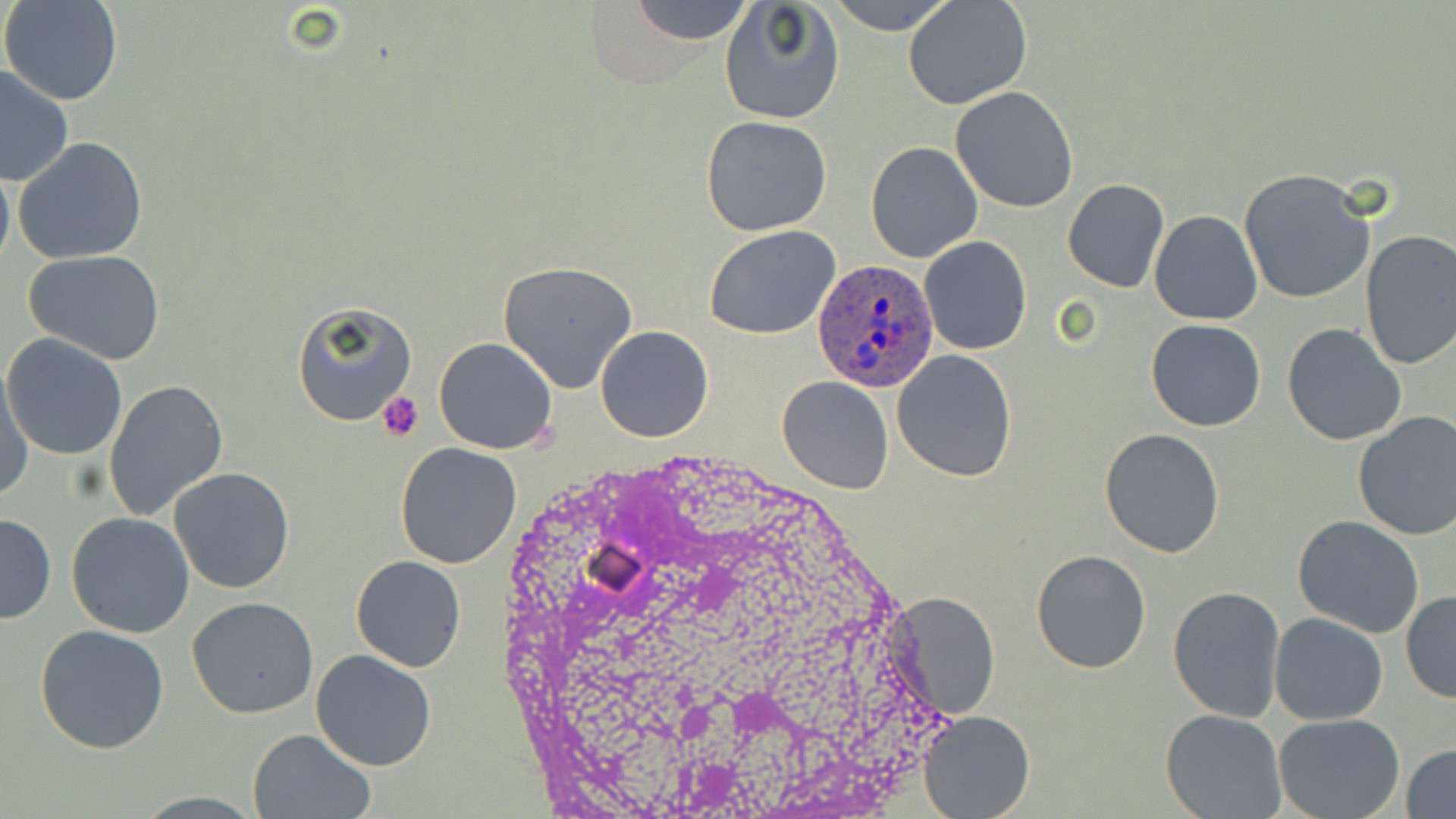
slide-level diagnosis = Plasmodium ovale
uninfected red blood cell locations = approximate bounding boxes as (x1, y1, x2, y2) in pixels: (2, 0, 124, 107), (628, 0, 755, 44), (826, 0, 958, 36), (904, 0, 1033, 109), (718, 2, 845, 125), (0, 65, 76, 188), (949, 86, 1079, 213), (700, 115, 833, 237), (14, 137, 148, 264), (865, 141, 983, 263), (0, 164, 14, 273), (1238, 168, 1376, 305), (1062, 178, 1170, 292), (1150, 211, 1262, 326), (704, 225, 841, 340), (1357, 229, 1456, 371), (920, 236, 1032, 356), (25, 250, 166, 365), (498, 261, 641, 394), (290, 299, 416, 427), (1147, 320, 1265, 432), (1281, 324, 1406, 446), (594, 326, 713, 443), (2, 334, 129, 462), (433, 337, 558, 455), (892, 349, 1018, 481), (1, 368, 33, 500), (776, 376, 893, 495), (105, 379, 228, 521), (1352, 411, 1456, 540), (1098, 428, 1224, 558), (395, 442, 522, 569), (169, 465, 294, 595), (0, 513, 55, 624), (66, 513, 195, 639), (1293, 516, 1425, 639), (1031, 549, 1151, 674), (351, 556, 466, 672), (1168, 584, 1286, 722), (887, 592, 1001, 721), (1401, 592, 1456, 704), (186, 598, 318, 720), (1269, 612, 1390, 726), (35, 626, 170, 754), (310, 648, 437, 770), (918, 709, 1035, 819), (1161, 709, 1288, 819), (1273, 713, 1404, 819), (248, 729, 375, 818), (1403, 742, 1456, 818)
stain = May-Grünwald-Giemsa
magnification = 1000x
modality = optical microscopy
preparation = thin blood film
Plasmodium ovale-infected red blood cell locations = approximate bounding boxes as (x1, y1, x2, y2) in pixels: (809, 257, 940, 391)
image size = 1456×819 pixels
platelet locations = approximate bounding boxes as (x1, y1, x2, y2) in pixels: (376, 390, 424, 440)
field of view = single